Report the malaria status of this cell.
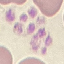

Parasitized.

preparation = thin blood film
stain = Giemsa
capture = smartphone through the microscope eyepiece
image type = automatically extracted cell patch, resized to 64 × 64 pixels